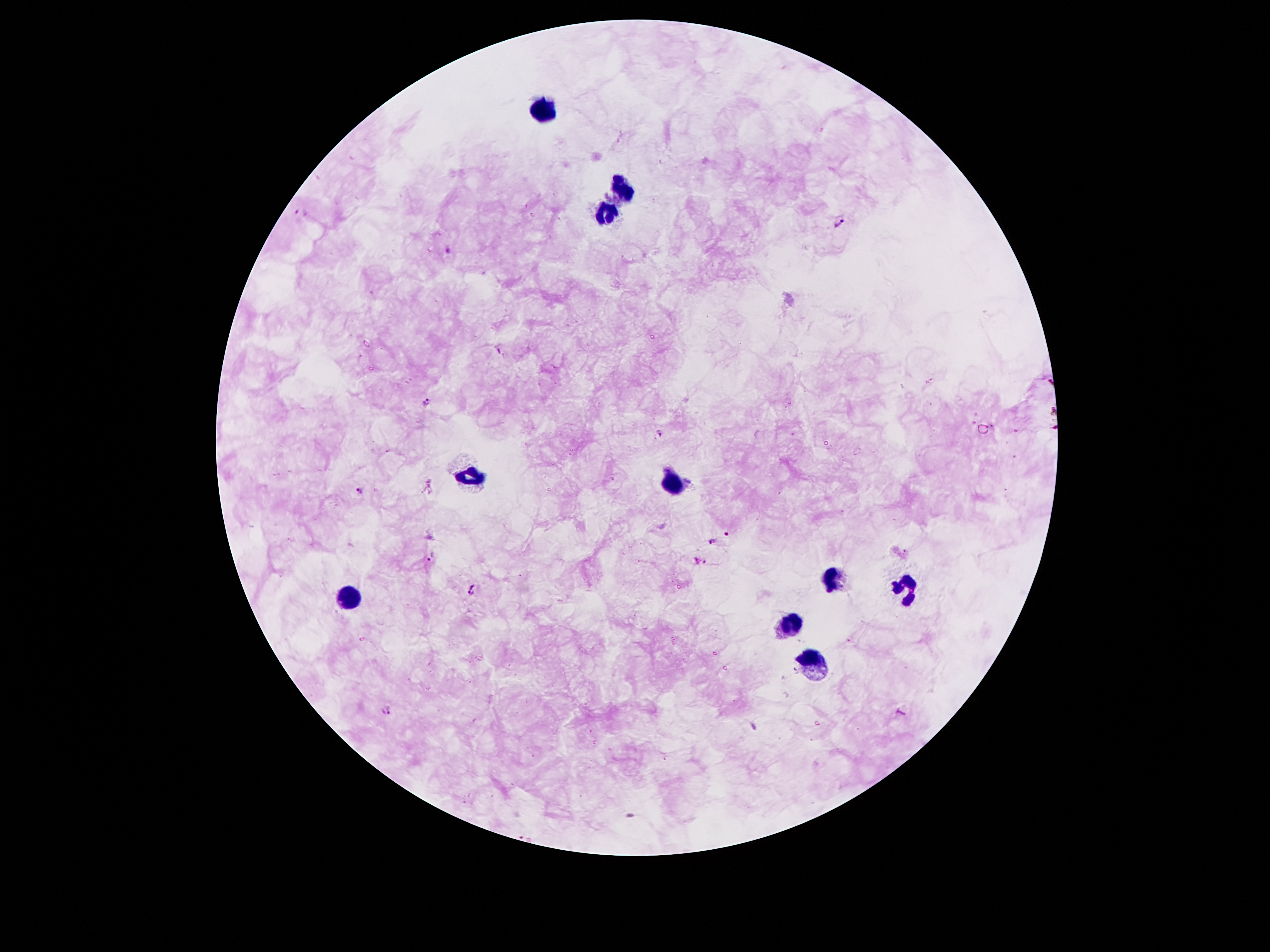 Approximate centers as {x, y} in pixels. Leukocyte locations: {543, 110}, {619, 188}, {604, 214}, {472, 478}, {673, 480}, {831, 578}, {912, 588}, {350, 595}, {788, 624}, {812, 664}. Malaria parasite locations: {300, 215}, {840, 221}, {449, 250}, {499, 349}, {427, 402}, {660, 435}, {357, 488}, {729, 535}, {713, 541}, {431, 556}, {701, 562}, {471, 588}, {386, 712}. Giemsa-stained preparation. Thick blood smear. Single field of view. Image is 1270×952 pixels. 100x magnification. Photographed through the microscope eyepiece with a smartphone camera. Patient malaria status: infected with Plasmodium falciparum.